Comment on the morphology of the erythrocytes.
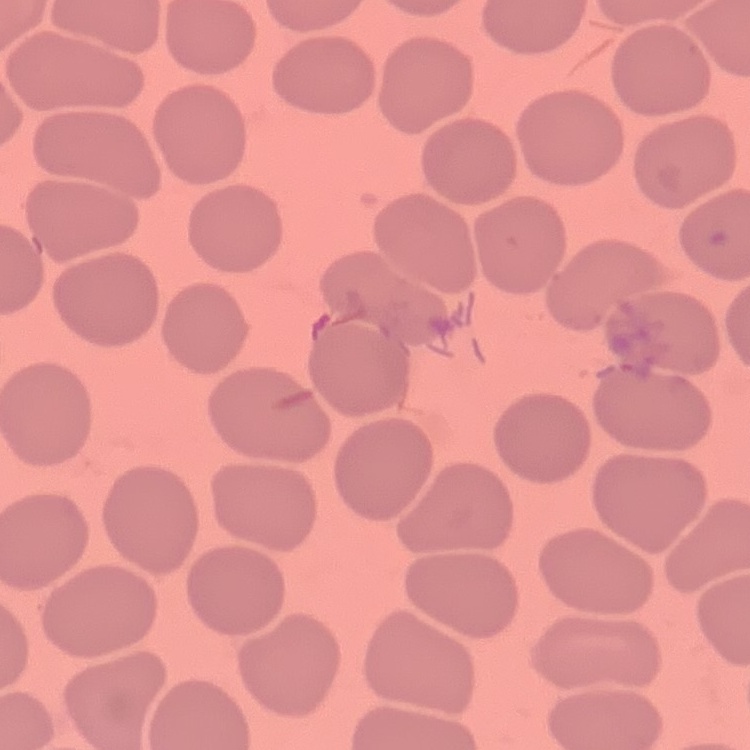

They show no rouleaux formation.

Summary:
  - Stain: Field's or Giemsa
  - Image type: square crop of a larger photomicrograph
  - Preparation: thin blood smear